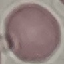 Result: no malaria parasites detected. Giemsa-stained preparation. Cell patch, automatically extracted from a larger field of view and resized to 64 × 64 pixels. Thin blood smear. Acquired by smartphone through the microscope eyepiece.